Locate every malaria parasite and every leukocyte.
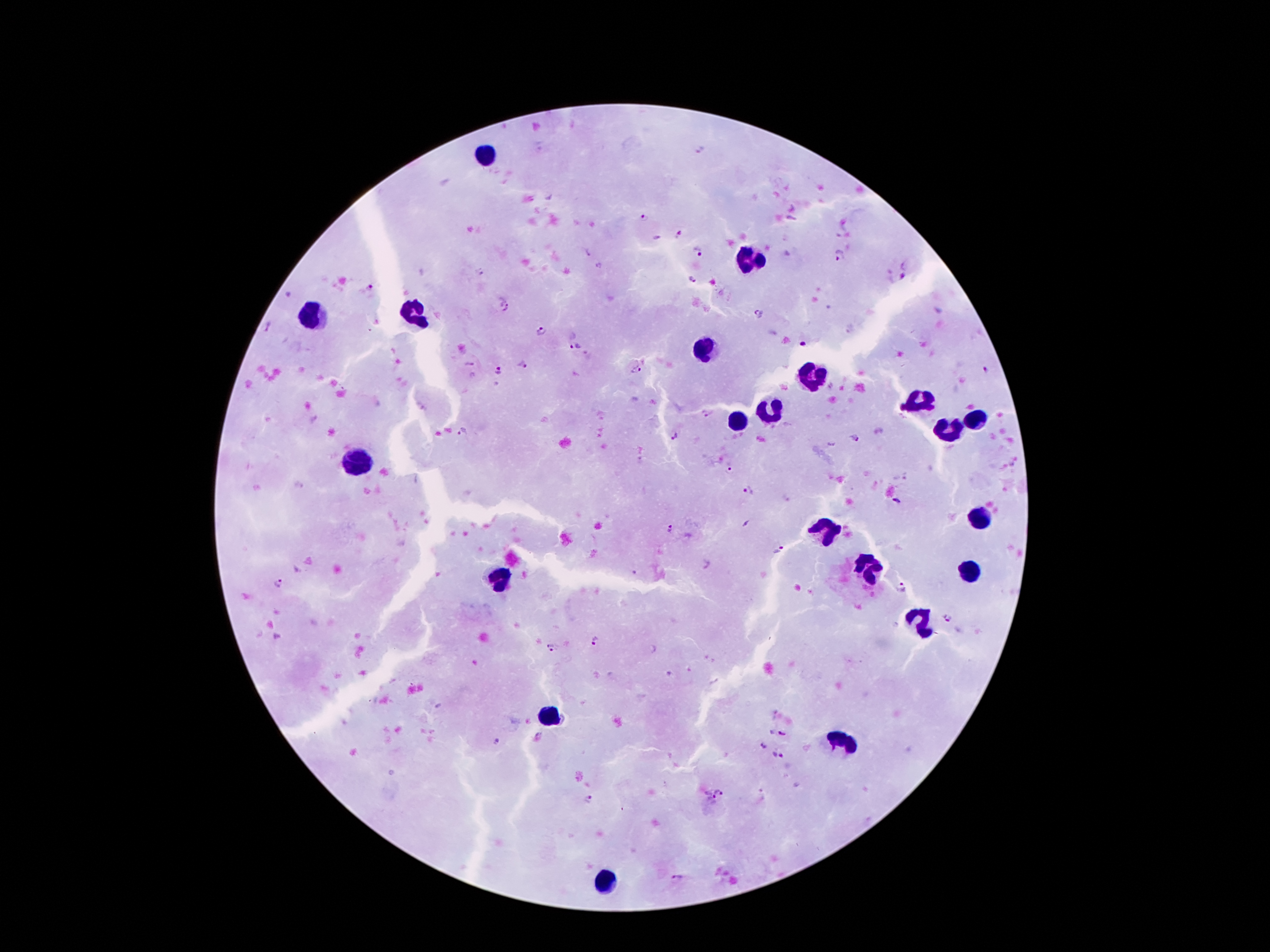

Approximate object centers, in pixels from the top-left corner.
Malaria parasites: (x=701, y=150), (x=643, y=218), (x=681, y=236), (x=698, y=252), (x=841, y=255), (x=481, y=274), (x=691, y=278), (x=897, y=281), (x=369, y=285), (x=505, y=308), (x=760, y=315), (x=269, y=326), (x=542, y=331), (x=804, y=344), (x=574, y=345), (x=469, y=364), (x=522, y=364), (x=497, y=369), (x=636, y=370), (x=985, y=373), (x=706, y=413), (x=465, y=431), (x=675, y=437), (x=855, y=437), (x=730, y=471), (x=749, y=490), (x=896, y=499), (x=670, y=530), (x=780, y=550), (x=278, y=582), (x=902, y=588), (x=948, y=619), (x=596, y=641), (x=553, y=649), (x=782, y=734), (x=496, y=741), (x=763, y=745), (x=777, y=755), (x=720, y=790), (x=708, y=796), (x=587, y=798), (x=677, y=878).
Leukocytes: (x=487, y=155), (x=748, y=263), (x=414, y=312), (x=308, y=319), (x=705, y=349), (x=810, y=375), (x=920, y=403), (x=772, y=409), (x=976, y=420), (x=737, y=422), (x=948, y=431), (x=362, y=459), (x=978, y=519), (x=825, y=530), (x=869, y=564), (x=970, y=569), (x=502, y=577), (x=920, y=627), (x=554, y=715), (x=845, y=741), (x=599, y=885).

Summary:
  - Preparation: thick peripheral-blood smear
  - Patient malaria status: infected with Plasmodium falciparum
  - Capture: smartphone camera through the microscope eyepiece
  - Image size: 1270×952 pixels
  - Magnification: 100x
  - Stain: Giemsa
  - Field of view: one from this slide